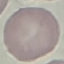

malaria_status: uninfected
capture: smartphone through the microscope eyepiece
stain: Giemsa
preparation: thin blood film
image_type: cell patch, automatically extracted from a larger field of view and resized to 64 × 64 pixels